State which cell type is depicted.
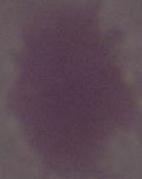

This is an erythrocyte.

1000x magnification. Micrograph.